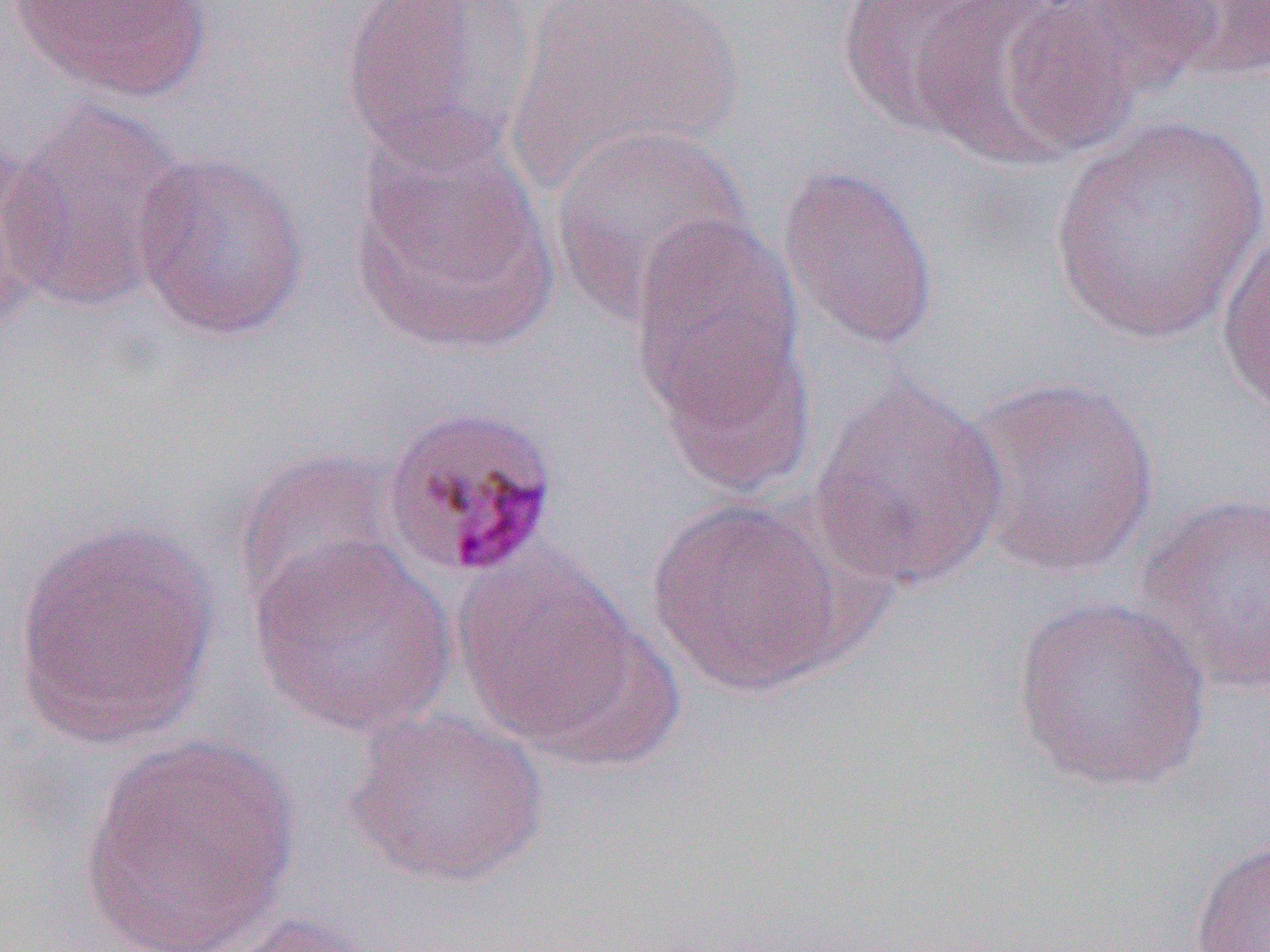
Summary:
  - Coordinate format: approximate bounding boxes as [x1, y1, x2, y2] in pixels
  - Uninfected red blood cell locations: [9, 0, 212, 102], [338, 0, 537, 173], [509, 0, 744, 191], [833, 0, 1010, 138], [1054, 0, 1222, 95], [1168, 0, 1270, 81], [913, 1, 1131, 168], [3, 99, 191, 314], [1047, 115, 1269, 348], [550, 123, 752, 322], [348, 124, 558, 355], [0, 150, 63, 327], [129, 150, 310, 341], [776, 162, 941, 355], [627, 214, 807, 438], [1216, 227, 1270, 422], [655, 324, 816, 502], [809, 372, 1010, 596], [962, 374, 1162, 579], [231, 448, 403, 615], [1135, 492, 1270, 697], [646, 496, 856, 696], [11, 516, 221, 754], [248, 534, 456, 738], [452, 549, 655, 760], [1010, 594, 1213, 793], [342, 707, 551, 889], [78, 734, 300, 950], [1189, 834, 1270, 951], [205, 913, 388, 952]
  - Slide-level diagnosis: Plasmodium malariae
  - Image size: 1270×952 pixels
  - Preparation: thin blood film
  - Modality: light microscopy
  - Field of view: single
  - Magnification: 1000x